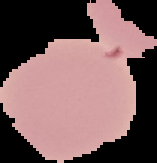
Summary:
  - Result: no Plasmodium parasites seen
  - Image size: 157×163 pixels
  - Preparation: thin blood film
  - Image type: cell region segmented out of the field of view; surrounding area masked to black